Identify the preparation type.
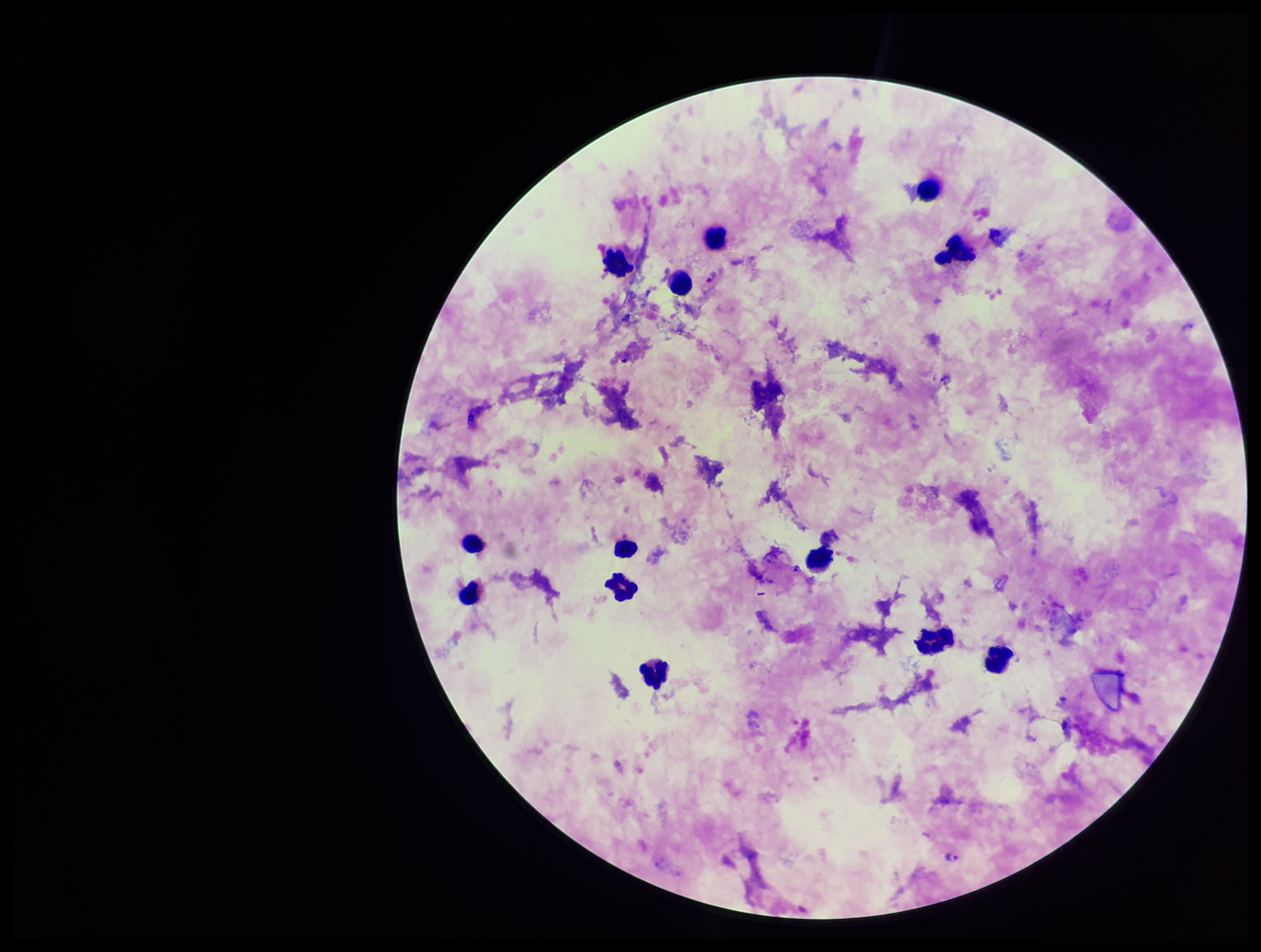
Thick.

Leukocyte count: 13. Image is 1261×952 pixels. Species reported for this patient: Plasmodium falciparum. Parasite count: 2. Smartphone photograph taken through the eyepiece of a microscope. One field from this slide. Giemsa stain. Plasmodium parasites: detected. Patient malaria status: infected.